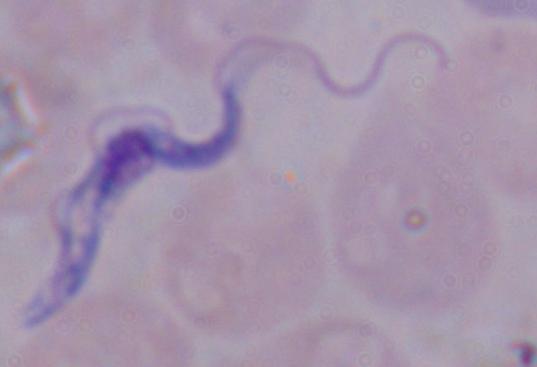 Photomicrograph. A trypanosome is seen. 1000x magnification.